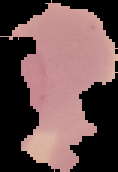
preparation = thin blood smear
image size = 118×172 pixels
result = no malaria parasites detected
image type = segmented cell region with the area outside set to black